Name the parasite shown.
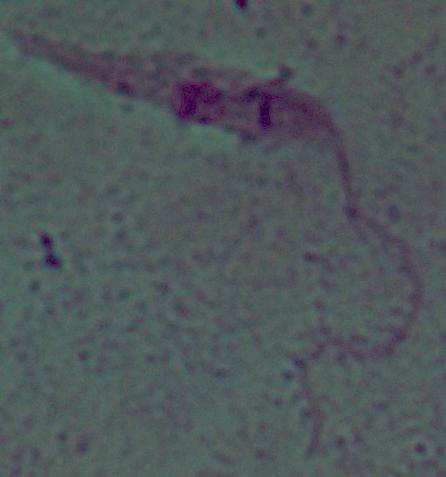

Leishmania.

Summary:
  - Modality: micrograph
  - Magnification: 1000x